Assess this cell for malaria.
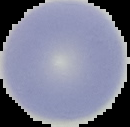
It is uninfected.

The area outside the segmented cell region is set to black. From a thin blood smear. Image is 130×127 pixels.